Classify this cell by malaria status.
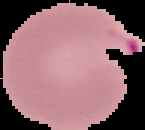

Parasitized.

Image is 145×130 pixels. From a thin blood smear. The area outside the segmented cell region is set to black.